Locate every uninfected red blood cell.
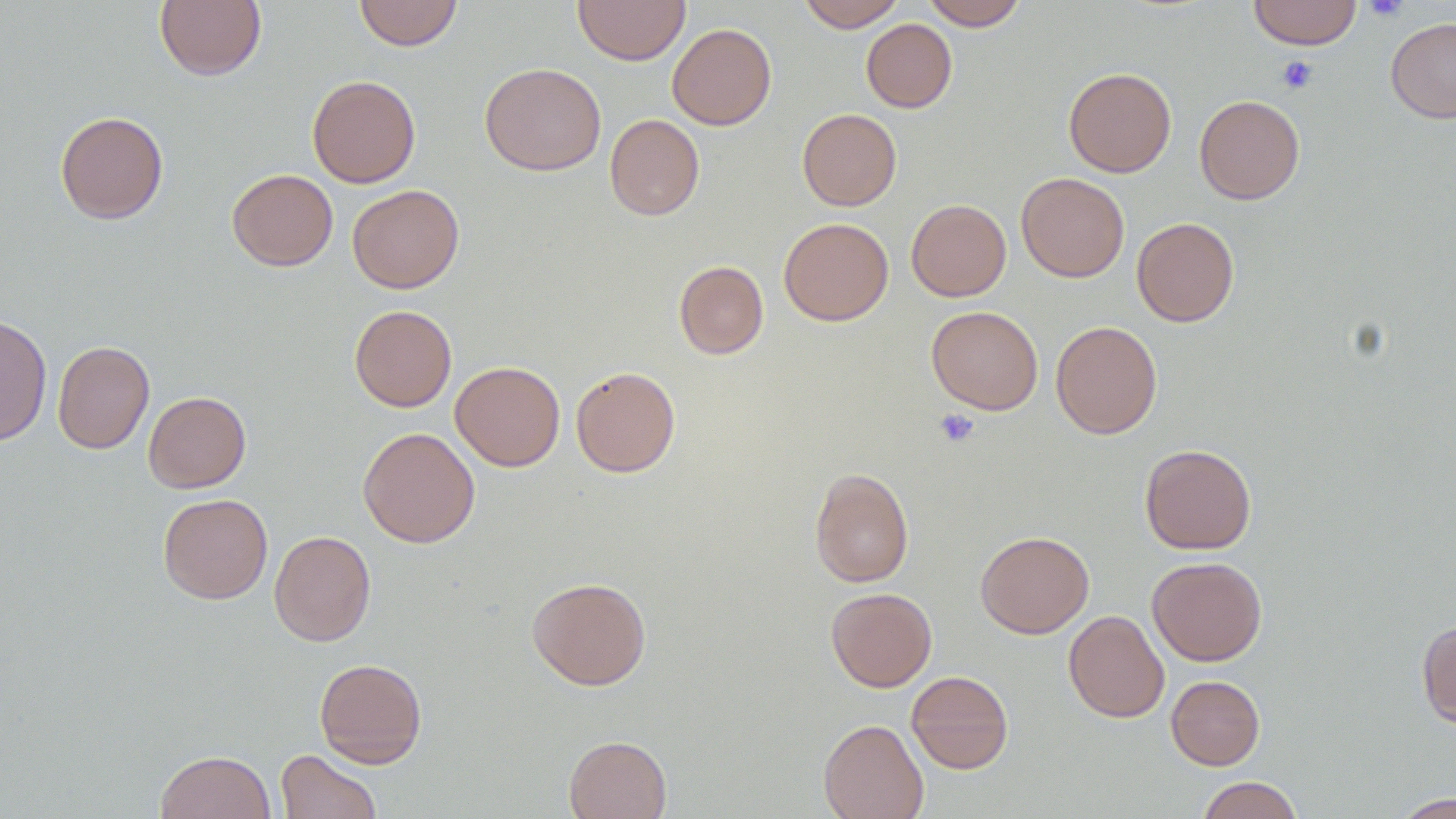
Approximate bounding boxes as (x1,y1)-(x2,y2) corner pairs in pixels.
Uninfected red blood cells: (353,0)-(463,51), (573,0)-(690,65), (798,0)-(906,32), (921,0)-(1028,30), (1248,0)-(1361,49), (154,1)-(267,81), (1386,17)-(1456,123), (861,19)-(957,112), (667,23)-(777,130), (479,62)-(606,176), (1063,67)-(1177,178), (307,74)-(421,188), (1194,95)-(1305,204), (797,108)-(901,211), (55,110)-(168,224), (604,114)-(705,220), (227,169)-(338,271), (1016,172)-(1129,282), (347,184)-(465,293), (906,199)-(1011,301), (778,217)-(894,326), (1131,217)-(1240,327), (674,261)-(768,359), (349,305)-(457,412), (926,306)-(1043,415), (0,313)-(52,447), (1051,320)-(1161,439), (52,340)-(154,454), (450,361)-(565,471), (570,366)-(681,477), (143,391)-(251,493), (357,426)-(480,548), (1140,443)-(1257,554), (809,467)-(914,587), (157,493)-(273,604), (270,530)-(376,646), (975,531)-(1094,638), (1146,556)-(1267,666), (526,576)-(652,690), (826,587)-(937,691), (1064,610)-(1169,723), (1416,619)-(1456,728), (314,658)-(428,768), (906,670)-(1013,774), (1166,675)-(1265,770), (818,718)-(929,819), (563,734)-(672,819), (276,749)-(382,819), (155,750)-(276,819), (1198,775)-(1304,819), (1388,793)-(1455,818).

{
  "slide_level_diagnosis": "no evidence of blood parasites",
  "modality": "light microscopy",
  "image_size": "1456×819 pixels",
  "platelet_locations": "approximate bounding boxes as (x1,y1)-(x2,y2) corner pairs in pixels: (1362,0)-(1409,21), (1277,55)-(1318,94), (934,409)-(980,447)",
  "magnification": "1000x",
  "field_of_view": "single",
  "preparation": "thin blood film"
}